Point out every malaria parasite and every leukocyte.
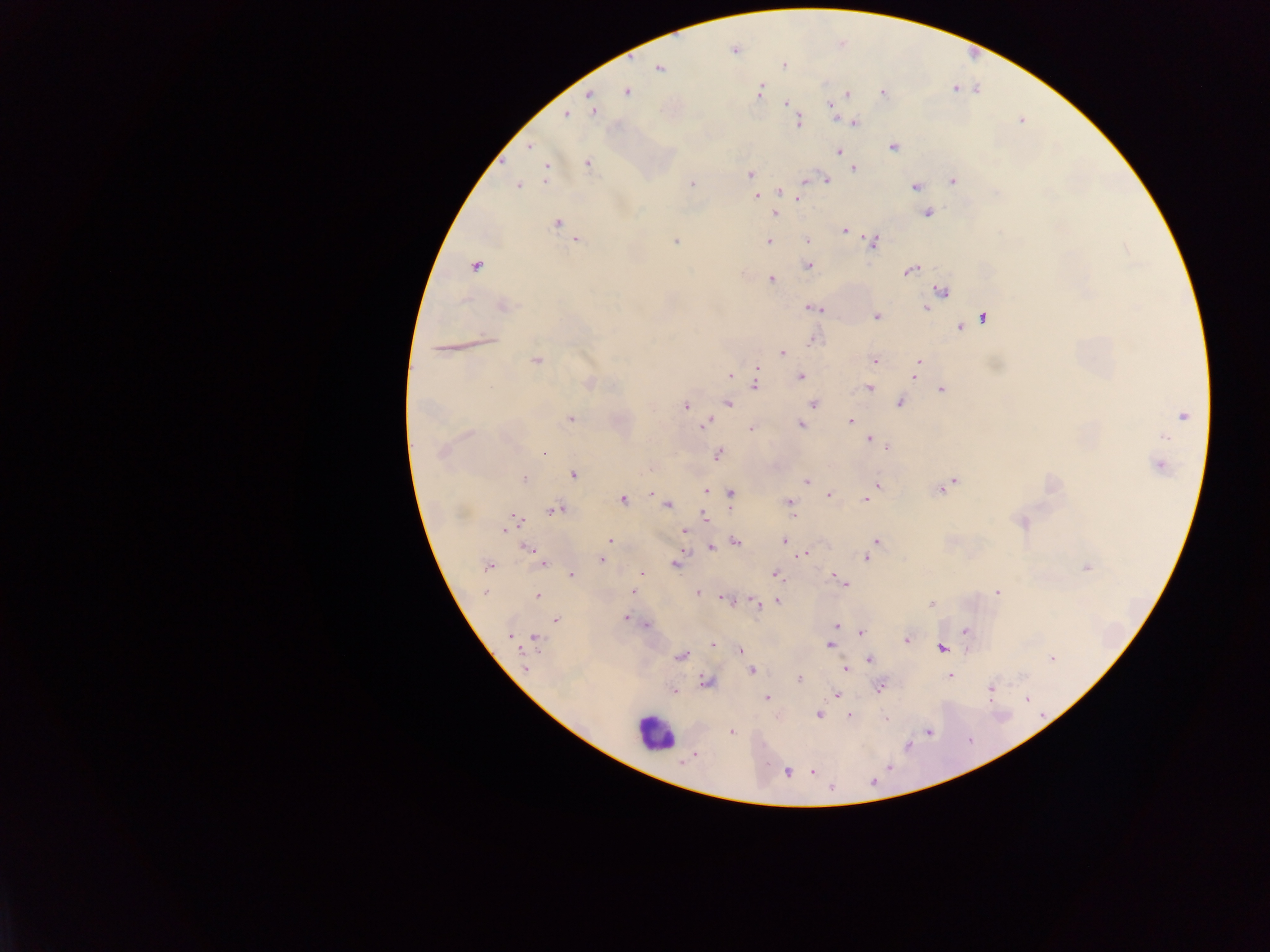
Approximate centers as {x, y} in pixels.
Malaria parasites: {734, 50}, {783, 66}, {659, 67}, {758, 91}, {626, 92}, {882, 92}, {847, 94}, {590, 96}, {786, 103}, {592, 108}, {830, 108}, {566, 115}, {796, 121}, {854, 121}, {529, 146}, {893, 146}, {838, 152}, {587, 163}, {853, 168}, {545, 169}, {750, 174}, {805, 180}, {826, 180}, {953, 181}, {517, 185}, {692, 185}, {915, 186}, {754, 189}, {780, 191}, {756, 196}, {798, 200}, {774, 212}, {927, 212}, {557, 223}, {843, 231}, {576, 240}, {807, 240}, {676, 241}, {768, 241}, {873, 241}, {808, 265}, {476, 266}, {911, 269}, {771, 280}, {941, 290}, {502, 306}, {809, 307}, {820, 308}, {924, 308}, {877, 316}, {983, 317}, {960, 327}, {814, 338}, {486, 340}, {781, 352}, {535, 360}, {874, 360}, {917, 361}, {757, 368}, {916, 368}, {730, 376}, {800, 376}, {915, 378}, {589, 382}, {755, 385}, {868, 388}, {941, 389}, {900, 401}, {728, 403}, {813, 403}, {685, 405}, {1183, 415}, {570, 419}, {851, 422}, {706, 423}, {800, 424}, {751, 428}, {1164, 437}, {867, 438}, {886, 446}, {442, 452}, {543, 452}, {718, 454}, {1159, 464}, {574, 474}, {524, 479}, {954, 480}, {806, 481}, {878, 485}, {945, 485}, {706, 490}, {730, 493}, {828, 495}, {621, 499}, {866, 500}, {667, 504}, {789, 504}, {554, 510}, {704, 515}, {791, 517}, {1021, 522}, {510, 524}, {683, 531}, {609, 541}, {784, 541}, {876, 541}, {735, 542}, {710, 546}, {530, 549}, {804, 554}, {536, 557}, {867, 557}, {601, 560}, {542, 563}, {676, 563}, {487, 566}, {1086, 566}, {774, 573}, {572, 574}, {642, 574}, {831, 575}, {843, 583}, {484, 592}, {633, 592}, {696, 592}, {996, 592}, {537, 596}, {726, 600}, {778, 600}, {754, 602}, {760, 604}, {931, 605}, {625, 617}, {556, 619}, {648, 623}, {837, 625}, {965, 631}, {861, 632}, {510, 635}, {535, 638}, {906, 640}, {711, 644}, {828, 644}, {941, 647}, {741, 650}, {681, 656}, {1051, 658}, {870, 660}, {524, 668}, {845, 669}, {751, 671}, {950, 676}, {798, 679}, {706, 682}, {880, 685}, {990, 689}, {674, 690}, {835, 694}, {767, 697}, {818, 714}, {849, 716}, {885, 717}, {731, 731}, {928, 731}, {694, 754}, {788, 771}, {811, 771}.
Leukocytes: {655, 732}.

Summary:
  - Image size: 1270×952 pixels
  - Country: Ghana
  - Capture: mobile-phone photograph through a microscope
  - Preparation: thick blood film
  - Field of view: single